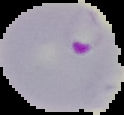
Summary:
  - Image type: segmented cell region with the area outside set to black
  - Preparation: thin blood smear
  - Malaria status: parasitized
  - Image size: 124×115 pixels